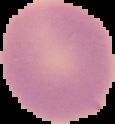
malaria_status: uninfected
preparation: thin blood film
image_type: segmented cell region on a black background
image_size: 115×124 pixels